Give the location of every parasitized RBC.
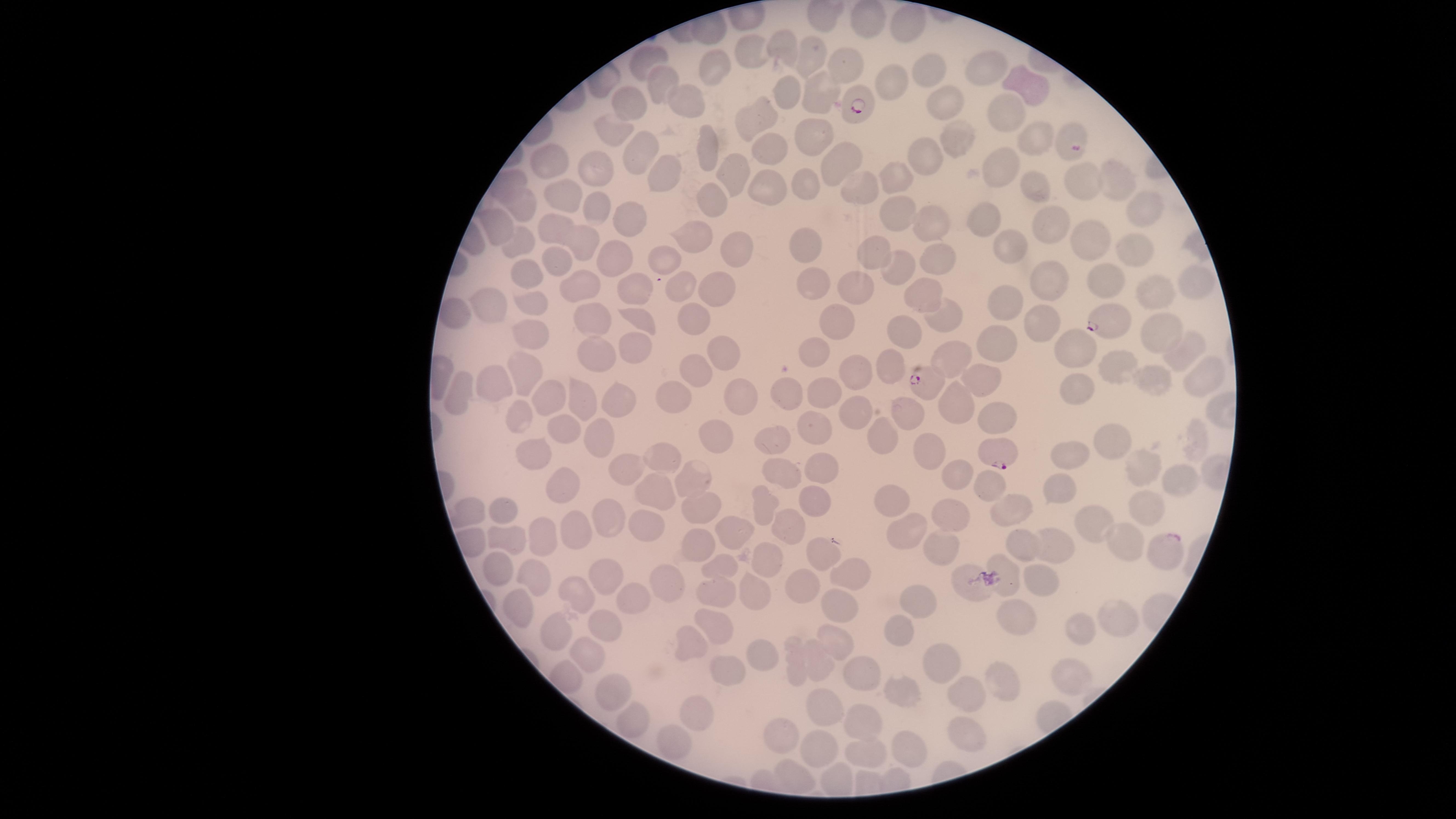

Approximate marker points as [x, y] in pixels.
Parasitized RBCs: [852, 102], [1069, 138], [1109, 323], [920, 381], [1001, 448], [1164, 554].

{
  "visible_region": "circular",
  "capture": "smartphone photograph through the microscope eyepiece",
  "field_of_view": "single",
  "uninfected_RBCs": "approximate marker points as [x, y] in pixels: [822, 19], [865, 20], [909, 25], [782, 44], [746, 49], [810, 54], [647, 61], [713, 67], [840, 68], [984, 69], [921, 74], [659, 82], [890, 82], [1023, 84], [782, 88], [818, 97], [687, 98], [946, 102], [633, 104], [1009, 109], [752, 123], [619, 130], [952, 136], [1039, 138], [812, 139], [768, 146], [704, 148], [553, 156], [638, 156], [832, 157], [924, 160], [1004, 166], [598, 170], [657, 174], [897, 176], [724, 178], [1118, 180], [1082, 182], [806, 186], [1038, 187], [770, 190], [862, 190], [565, 202], [592, 209], [520, 211], [706, 211], [1146, 211], [629, 218], [902, 218], [989, 222], [493, 223], [930, 226], [1049, 227], [550, 230], [518, 236], [688, 240], [1094, 241], [586, 243], [807, 244], [1131, 248], [1010, 250], [734, 251], [872, 254], [930, 256], [557, 257], [661, 261], [616, 263], [896, 269], [528, 274], [815, 282], [1107, 282], [1189, 283], [685, 285], [585, 286], [635, 287], [717, 287], [925, 289], [1049, 289], [859, 290], [1152, 294], [533, 296], [1009, 302], [489, 304], [454, 313], [695, 318], [1045, 319], [941, 320], [590, 322], [639, 322], [838, 327], [1161, 331], [531, 333], [902, 333], [999, 338], [635, 348], [722, 349], [1074, 349], [1182, 353], [956, 356], [811, 357], [894, 362], [596, 364], [1115, 367], [522, 372], [699, 372], [859, 376], [980, 376], [1203, 378], [1154, 381], [488, 383], [1077, 389], [550, 392], [823, 392], [742, 394], [790, 394], [464, 398], [624, 399], [673, 399], [582, 400], [958, 403], [856, 406], [902, 414], [522, 420], [997, 421], [815, 427], [565, 435], [717, 436], [883, 436], [773, 440], [601, 442], [1197, 443], [1119, 444], [931, 450], [531, 451], [661, 455], [1078, 455], [615, 469], [818, 469], [1182, 470], [779, 473], [953, 474], [1147, 474], [691, 477], [568, 480], [982, 482], [1059, 487], [652, 488], [890, 501], [763, 502], [812, 503], [1145, 505], [696, 507], [1009, 509], [499, 513], [469, 515], [601, 518], [957, 519], [637, 522], [787, 526], [571, 527], [1094, 528], [728, 532], [908, 535], [502, 536], [543, 536], [1118, 543], [1050, 545], [691, 547], [938, 547], [818, 550], [759, 552], [722, 566], [495, 569], [605, 573], [848, 573], [531, 574], [1010, 578], [802, 581], [1037, 582], [667, 586], [971, 587], [577, 591], [714, 595], [627, 596], [751, 596], [917, 599], [846, 603], [515, 608], [1020, 617], [1113, 617], [713, 626], [601, 627], [1082, 630], [902, 633], [558, 634], [837, 642], [688, 643], [759, 651], [585, 652], [940, 661], [819, 663], [794, 666], [733, 675], [860, 675], [1070, 676], [999, 688], [613, 691], [964, 693], [902, 694], [700, 705], [827, 710], [863, 722], [631, 723], [966, 735], [784, 736], [670, 743], [907, 746], [815, 750], [865, 750], [791, 772]",
  "stain": "Giemsa",
  "species": "Plasmodium falciparum",
  "preparation": "thin blood smear",
  "image_size": "1456×819 pixels"
}